Locate every Plasmodium parasite.
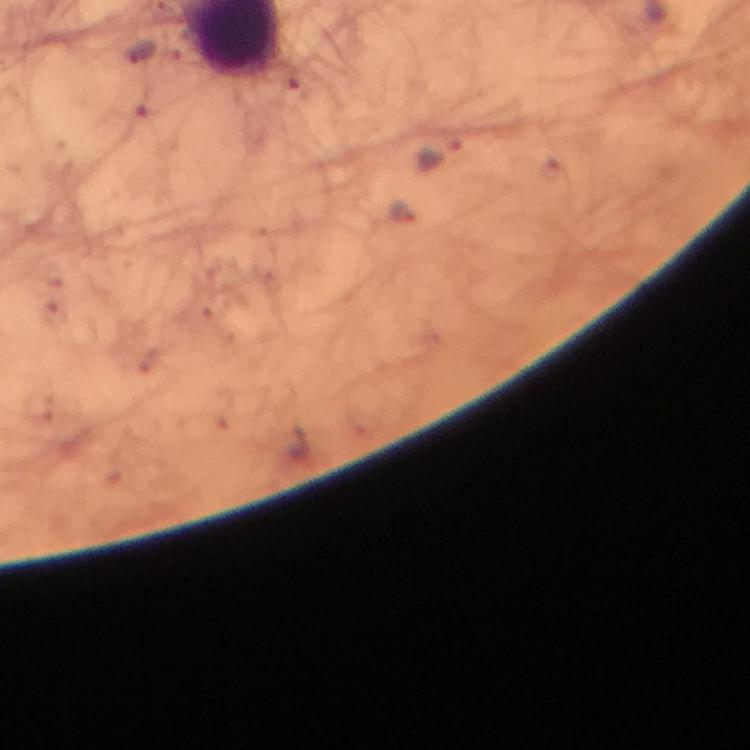
Approximate centers as (x, y) in pixels.
Plasmodium parasites: (138, 52), (441, 154), (402, 211).

image size = 750×750 pixels
cropped from = one field of view
stain = Giemsa
context = from a diagnostic examination for malaria
magnification = 100x
immersion oil = used
capture = smartphone photograph through a microscope
preparation = thick smear